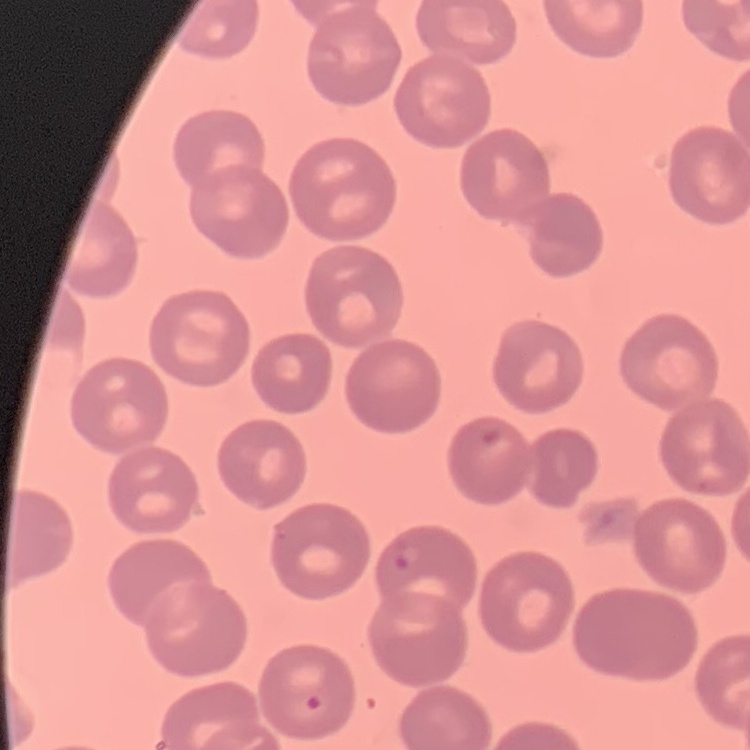
Summary:
  - Red blood cell morphology: no rouleaux formation
  - Preparation: thin blood film
  - Stain: Field's or Giemsa
  - Image type: one tile cut from a larger photomicrograph